Assess this cell for malaria.
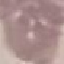
It is uninfected.

Summary:
  - Image type: automatically extracted cell patch, resized to 64 × 64 pixels
  - Preparation: thin blood smear
  - Capture: smartphone camera at the microscope eyepiece
  - Stain: Giemsa